Locate every uninfected red blood cell.
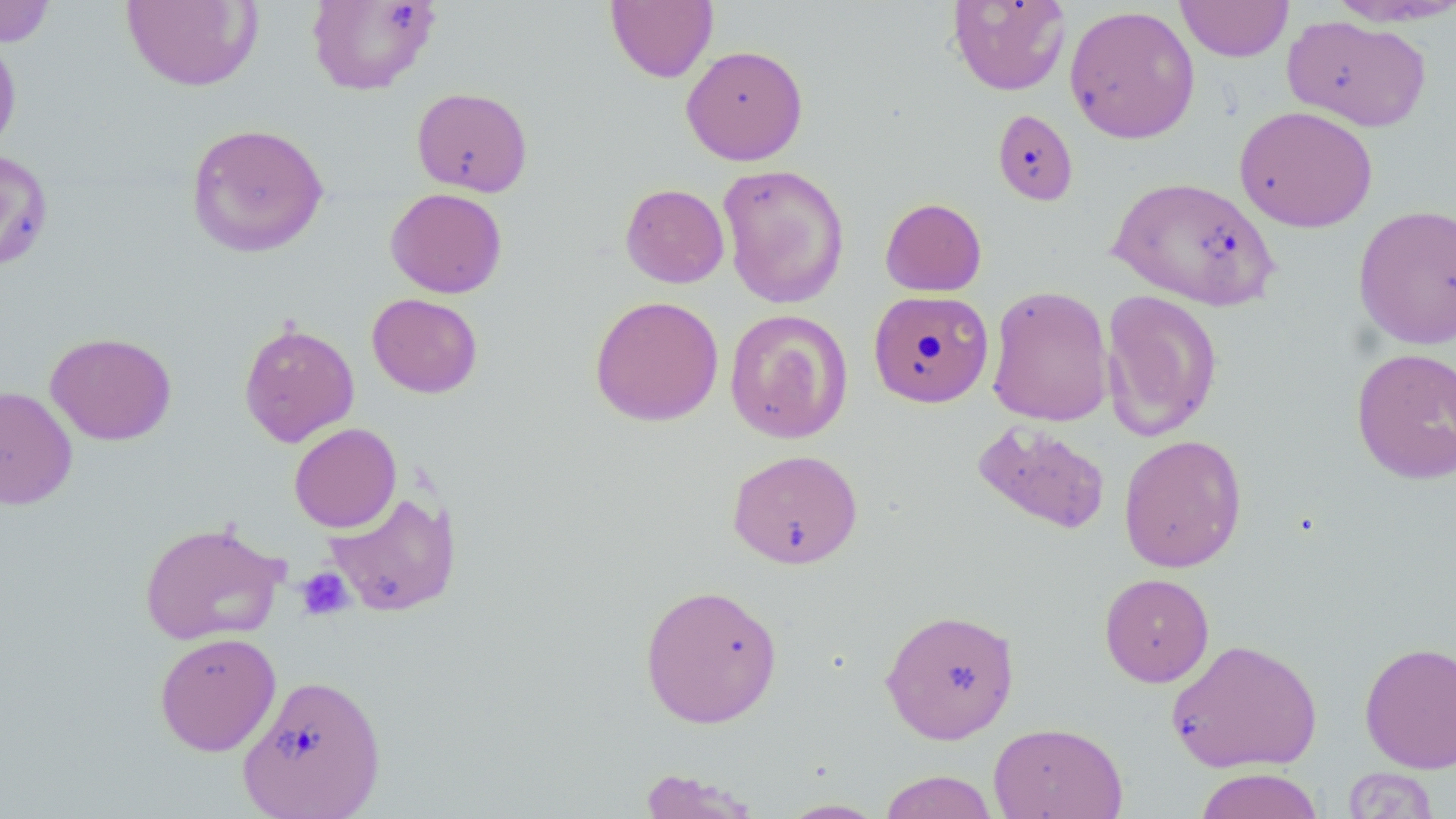
Approximate bounding boxes as named x1/y1/x2/y2 corners in pixels.
Uninfected red blood cells: (x1=605, y1=0, x2=718, y2=83), (x1=1175, y1=0, x2=1294, y2=62), (x1=1325, y1=0, x2=1456, y2=27), (x1=0, y1=1, x2=58, y2=47), (x1=121, y1=1, x2=263, y2=92), (x1=307, y1=1, x2=439, y2=95), (x1=947, y1=1, x2=1071, y2=96), (x1=1064, y1=4, x2=1200, y2=144), (x1=1282, y1=15, x2=1431, y2=132), (x1=0, y1=33, x2=22, y2=154), (x1=681, y1=44, x2=808, y2=165), (x1=412, y1=87, x2=532, y2=197), (x1=1234, y1=105, x2=1378, y2=232), (x1=992, y1=109, x2=1078, y2=205), (x1=186, y1=122, x2=329, y2=258), (x1=0, y1=150, x2=53, y2=271), (x1=718, y1=163, x2=850, y2=309), (x1=1109, y1=175, x2=1281, y2=310), (x1=620, y1=183, x2=729, y2=288), (x1=385, y1=188, x2=507, y2=298), (x1=880, y1=197, x2=987, y2=296), (x1=1353, y1=204, x2=1456, y2=349), (x1=987, y1=285, x2=1113, y2=427), (x1=868, y1=290, x2=994, y2=408), (x1=1101, y1=290, x2=1223, y2=441), (x1=367, y1=293, x2=483, y2=398), (x1=589, y1=295, x2=724, y2=426), (x1=724, y1=308, x2=853, y2=443), (x1=238, y1=321, x2=360, y2=448), (x1=45, y1=331, x2=177, y2=445), (x1=1351, y1=347, x2=1456, y2=485), (x1=0, y1=386, x2=78, y2=510), (x1=973, y1=419, x2=1111, y2=535), (x1=288, y1=422, x2=401, y2=533), (x1=1118, y1=434, x2=1247, y2=573), (x1=727, y1=449, x2=863, y2=569), (x1=323, y1=490, x2=461, y2=618), (x1=139, y1=521, x2=287, y2=646), (x1=1099, y1=573, x2=1214, y2=687), (x1=639, y1=583, x2=783, y2=729), (x1=880, y1=608, x2=1019, y2=744), (x1=154, y1=632, x2=281, y2=756), (x1=1166, y1=637, x2=1322, y2=774), (x1=1359, y1=641, x2=1456, y2=774), (x1=237, y1=673, x2=386, y2=819), (x1=988, y1=721, x2=1127, y2=819), (x1=1193, y1=767, x2=1325, y2=819), (x1=1341, y1=767, x2=1440, y2=818), (x1=637, y1=768, x2=763, y2=818), (x1=878, y1=769, x2=1000, y2=819), (x1=775, y1=798, x2=890, y2=818).

{
  "slide_level_diagnosis": "no evidence of blood parasites",
  "magnification": "1000x",
  "stain": "May-Grünwald-Giemsa",
  "preparation": "thin blood film",
  "platelet_locations": "approximate bounding boxes as named x1/y1/x2/y2 corners in pixels: (x1=295, y1=567, x2=354, y2=621)",
  "modality": "light microscopy",
  "image_size": "1456×819 pixels",
  "field_of_view": "single"
}